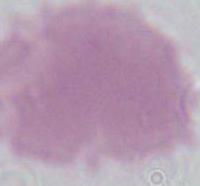

magnification = 1000x
identification = erythrocyte
modality = micrograph